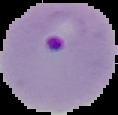
Result: Plasmodium parasites identified. Image is 118×115 pixels. From a thin blood smear. Cell region segmented out of the field of view; the surrounding area is masked to black.